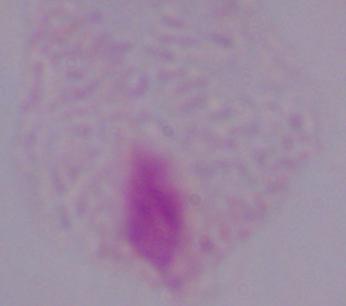

Micrograph. A trichomonad is seen. 1000x magnification.